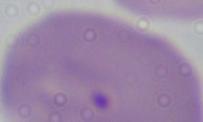
identification = Babesia
modality = photomicrograph
magnification = 1000x